Locate and identify every blood parasite.
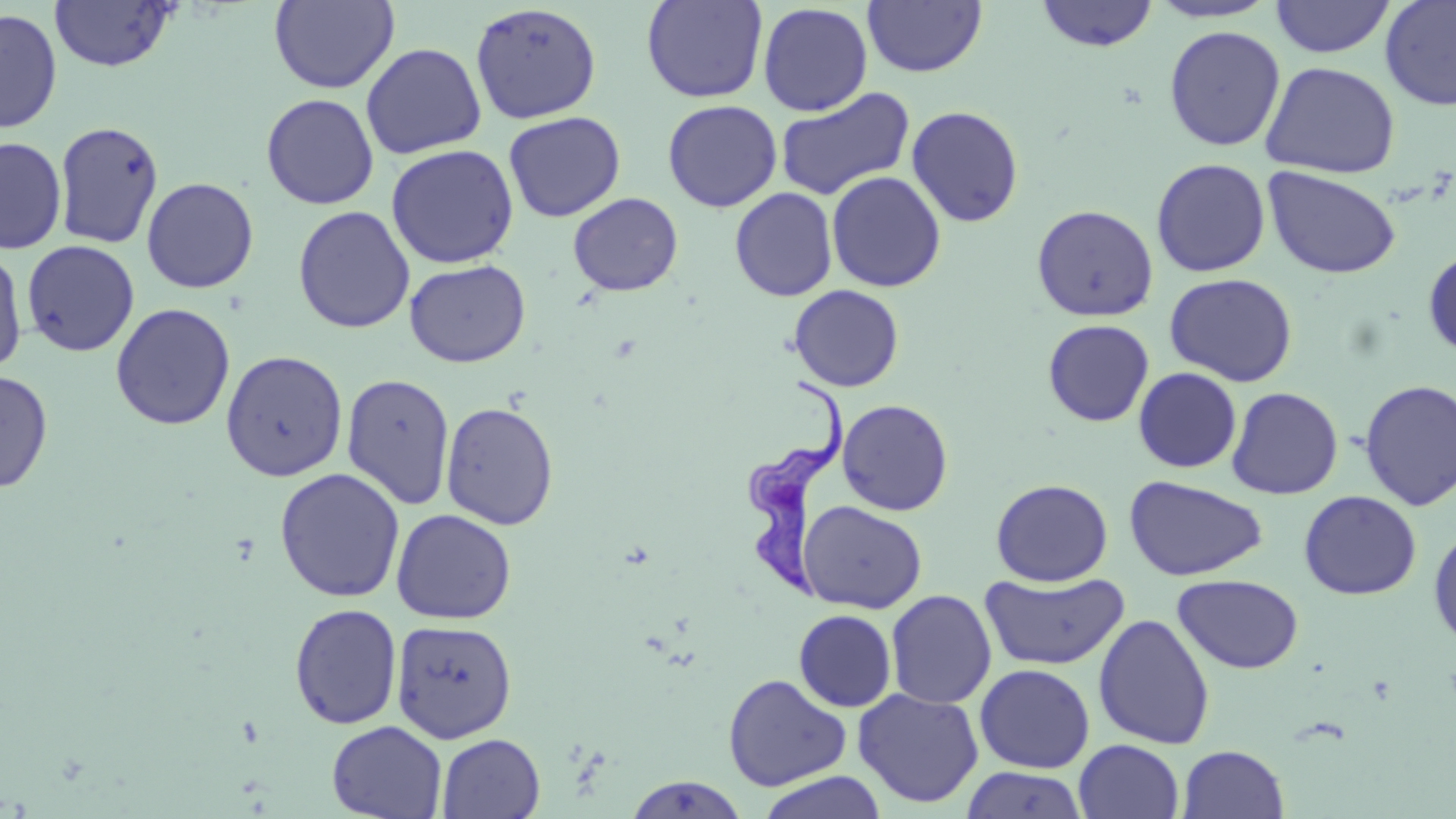
Approximate bounding boxes as [x1, y1, x2, y2] in pixels.
Trypanosoma brucei: [749, 377, 848, 605].
No Plasmodium falciparum, Plasmodium ovale, Plasmodium malariae, Plasmodium vivax, or Babesia divergens observed.

Summary:
  - Uninfected red blood cell locations: [48, 0, 179, 73], [269, 0, 399, 93], [641, 0, 767, 103], [1146, 0, 1281, 24], [1380, 0, 1456, 111], [863, 1, 987, 77], [1035, 1, 1159, 52], [1270, 1, 1396, 59], [470, 3, 602, 124], [757, 3, 873, 116], [0, 7, 62, 134], [1164, 25, 1286, 152], [361, 42, 486, 159], [1260, 61, 1401, 178], [774, 86, 915, 201], [261, 93, 379, 210], [662, 99, 783, 213], [906, 105, 1024, 228], [503, 111, 625, 222], [54, 121, 164, 249], [0, 136, 66, 254], [385, 144, 519, 269], [1151, 158, 1271, 278], [1263, 166, 1402, 280], [826, 171, 947, 292], [141, 177, 259, 294], [729, 187, 838, 301], [567, 192, 683, 296], [1031, 204, 1158, 322], [293, 205, 415, 333], [21, 240, 140, 357], [0, 246, 28, 376], [1423, 246, 1456, 360], [404, 259, 531, 368], [1164, 272, 1298, 387], [788, 284, 905, 392], [111, 303, 235, 431], [1042, 319, 1155, 426], [221, 350, 348, 481], [1133, 367, 1242, 473], [0, 370, 54, 493], [342, 373, 455, 510], [1357, 379, 1456, 511], [1227, 386, 1344, 499], [837, 399, 954, 516], [440, 401, 559, 529], [274, 468, 405, 603], [1124, 475, 1268, 582], [990, 478, 1113, 586], [1299, 490, 1421, 600], [797, 500, 927, 614], [391, 508, 517, 624], [1428, 526, 1456, 650], [980, 571, 1130, 670], [1172, 574, 1304, 674], [885, 589, 997, 709], [289, 603, 403, 729], [793, 609, 897, 712], [1093, 613, 1215, 750], [390, 620, 518, 744], [974, 664, 1095, 773], [722, 673, 852, 792], [853, 688, 984, 808], [326, 720, 447, 819], [436, 733, 545, 818], [1073, 739, 1185, 819], [1178, 744, 1289, 818], [960, 766, 1089, 819], [755, 771, 888, 819], [622, 775, 750, 818]
  - Slide-level diagnosis: Trypanosoma brucei
  - Image size: 1456×819 pixels
  - Preparation: thin blood smear
  - Stain: May-Grünwald-Giemsa
  - Magnification: 1000x
  - Field of view: one of a larger specimen
  - Modality: light microscopy